Report the malaria status of this cell.
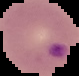

Parasitized.

The area outside the segmented cell region is set to black. Image is 79×76 pixels. From a thin blood film.